Assess this cell for malaria.
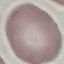
Uninfected.

Giemsa-stained preparation. Cell patch, automatically extracted from a larger field of view and resized to 64 × 64 pixels. Thin blood film. Photographed with a smartphone camera at the microscope eyepiece.